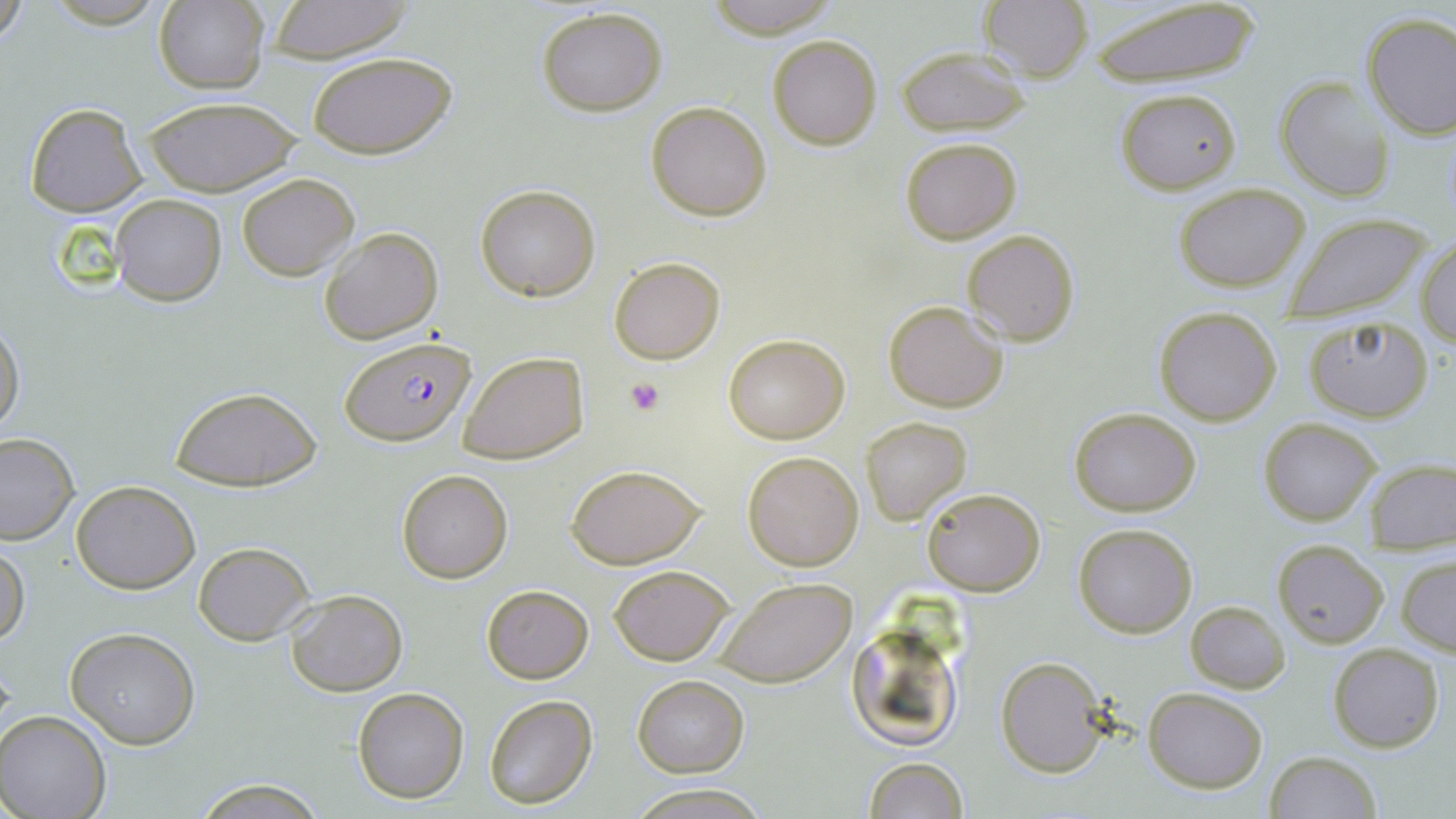 Approximate bounding boxes as (x1, y1, x2, y2) in pixels. Platelet locations: (626, 378, 666, 415). Uninfected red blood cell locations: (0, 0, 30, 48), (154, 1, 269, 94), (263, 1, 415, 63), (980, 1, 1094, 82), (701, 2, 842, 38), (1089, 3, 1261, 88), (536, 6, 668, 117), (1360, 12, 1456, 138), (767, 34, 884, 151), (897, 45, 1031, 135), (307, 53, 455, 159), (1274, 76, 1395, 203), (1114, 88, 1240, 194), (137, 95, 302, 198), (646, 100, 773, 220), (25, 103, 145, 217), (899, 137, 1022, 244), (237, 173, 358, 281), (1172, 182, 1313, 293), (475, 184, 601, 300), (111, 194, 227, 307), (1283, 212, 1433, 323), (319, 227, 443, 345), (963, 228, 1080, 346), (1417, 234, 1455, 345), (609, 255, 725, 364), (883, 299, 1009, 413), (1153, 308, 1284, 426), (0, 318, 24, 435), (1303, 318, 1435, 423), (723, 332, 850, 443), (459, 351, 589, 464), (171, 386, 319, 492), (1068, 407, 1202, 514), (863, 416, 971, 525), (1259, 417, 1380, 526), (0, 433, 79, 545), (742, 451, 864, 572), (1367, 459, 1456, 550), (566, 465, 706, 568), (396, 468, 514, 584), (71, 479, 201, 593), (922, 488, 1046, 596), (1073, 523, 1197, 638), (1272, 540, 1389, 647), (0, 542, 28, 650), (193, 542, 314, 645), (1398, 553, 1456, 655), (610, 564, 734, 666), (715, 577, 857, 687), (481, 584, 593, 684), (286, 588, 408, 697), (1186, 600, 1290, 694), (845, 615, 968, 752), (65, 627, 201, 749), (1328, 643, 1445, 752), (994, 655, 1111, 778), (632, 674, 749, 776), (352, 686, 469, 804), (1143, 686, 1269, 793), (483, 693, 597, 810), (1, 712, 113, 819), (1266, 751, 1380, 819), (861, 756, 971, 819), (189, 777, 329, 817), (628, 785, 768, 817). Plasmodium falciparum-infected red blood cell locations: (340, 334, 476, 447). Slide-level diagnosis: Plasmodium falciparum. Optical microscopy. Thin blood film. 1000x magnification. May-Grünwald-Giemsa-stained preparation. Single field of view. Image is 1456×819 pixels.